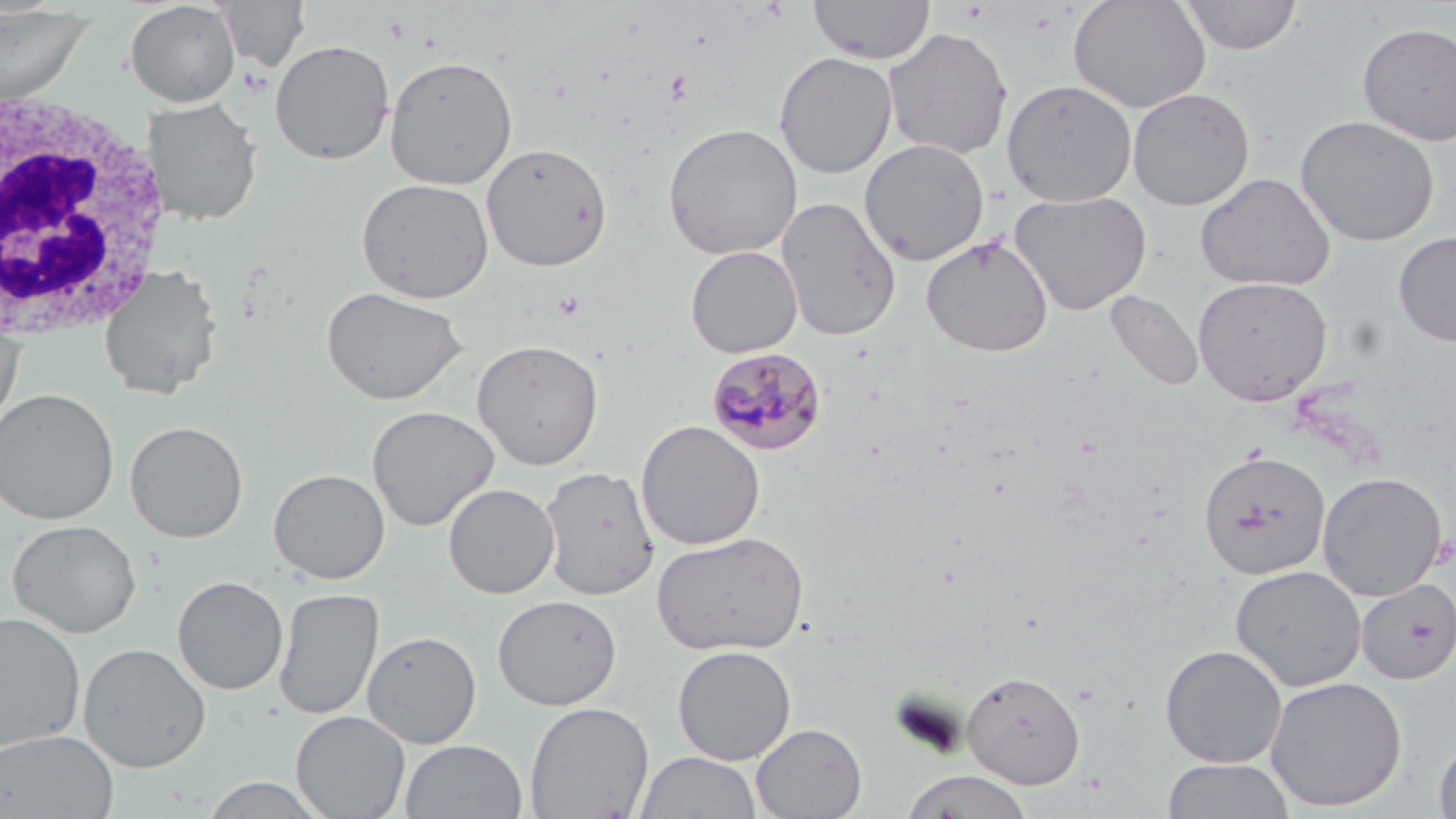 Approximate bounding boxes as named x1/y1/x2/y2 corners in pixels. White blood cell locations: (x1=0, y1=86, x2=171, y2=346). Platelet locations: (x1=665, y1=69, x2=692, y2=104), (x1=553, y1=291, x2=586, y2=320). Uninfected red blood cell locations: (x1=217, y1=0, x2=310, y2=72), (x1=809, y1=0, x2=935, y2=64), (x1=1069, y1=0, x2=1210, y2=113), (x1=1180, y1=0, x2=1301, y2=54), (x1=124, y1=1, x2=241, y2=107), (x1=0, y1=5, x2=96, y2=106), (x1=1356, y1=23, x2=1456, y2=145), (x1=883, y1=27, x2=1013, y2=161), (x1=269, y1=39, x2=395, y2=165), (x1=774, y1=51, x2=898, y2=179), (x1=384, y1=55, x2=517, y2=189), (x1=1001, y1=78, x2=1137, y2=207), (x1=1127, y1=87, x2=1255, y2=211), (x1=142, y1=98, x2=263, y2=227), (x1=1295, y1=114, x2=1439, y2=247), (x1=663, y1=122, x2=803, y2=260), (x1=859, y1=138, x2=989, y2=266), (x1=480, y1=142, x2=613, y2=272), (x1=1195, y1=172, x2=1336, y2=292), (x1=356, y1=177, x2=494, y2=303), (x1=1009, y1=189, x2=1152, y2=315), (x1=775, y1=196, x2=902, y2=341), (x1=1394, y1=231, x2=1456, y2=347), (x1=921, y1=235, x2=1054, y2=357), (x1=685, y1=245, x2=803, y2=358), (x1=97, y1=264, x2=224, y2=401), (x1=1192, y1=276, x2=1333, y2=405), (x1=321, y1=285, x2=469, y2=405), (x1=1106, y1=291, x2=1204, y2=391), (x1=0, y1=322, x2=24, y2=438), (x1=472, y1=339, x2=604, y2=470), (x1=0, y1=388, x2=119, y2=525), (x1=366, y1=404, x2=499, y2=531), (x1=636, y1=420, x2=766, y2=550), (x1=125, y1=421, x2=248, y2=543), (x1=1198, y1=448, x2=1331, y2=580), (x1=539, y1=465, x2=660, y2=601), (x1=268, y1=468, x2=390, y2=584), (x1=1317, y1=472, x2=1447, y2=600), (x1=443, y1=483, x2=560, y2=599), (x1=6, y1=519, x2=141, y2=638), (x1=650, y1=530, x2=810, y2=656), (x1=1230, y1=564, x2=1366, y2=691), (x1=172, y1=575, x2=289, y2=695), (x1=1355, y1=578, x2=1456, y2=685), (x1=274, y1=587, x2=384, y2=721), (x1=492, y1=594, x2=622, y2=710), (x1=0, y1=611, x2=86, y2=752), (x1=362, y1=630, x2=481, y2=748), (x1=77, y1=642, x2=212, y2=773), (x1=1159, y1=644, x2=1288, y2=768), (x1=672, y1=645, x2=796, y2=765), (x1=962, y1=670, x2=1085, y2=788), (x1=1265, y1=675, x2=1407, y2=812), (x1=525, y1=701, x2=655, y2=819), (x1=291, y1=710, x2=411, y2=819), (x1=751, y1=723, x2=867, y2=818), (x1=1, y1=729, x2=120, y2=819), (x1=1433, y1=735, x2=1456, y2=819), (x1=399, y1=739, x2=528, y2=819), (x1=634, y1=750, x2=762, y2=818), (x1=1160, y1=757, x2=1297, y2=819), (x1=899, y1=769, x2=1035, y2=819), (x1=198, y1=775, x2=332, y2=818). Plasmodium malariae-infected red blood cell locations: (x1=707, y1=347, x2=827, y2=456). Slide-level diagnosis: Plasmodium malariae. Image is 1456×819 pixels. Optical microscopy. Thin blood film. One field of a larger specimen. Captured at 1000x magnification. May-Grünwald-Giemsa-stained preparation.